Report the malaria status of this cell.
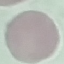

Uninfected.

Photographed with a smartphone camera at the microscope eyepiece. Thin smear of blood. Giemsa stain. Cell patch, automatically extracted from a larger field of view and resized to 64 × 64 pixels.